Assess this cell for malaria.
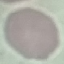
Uninfected.

image type = automatically extracted cell patch, resized to 64 × 64 pixels
capture = smartphone through the microscope eyepiece
stain = Giemsa
preparation = thin blood film